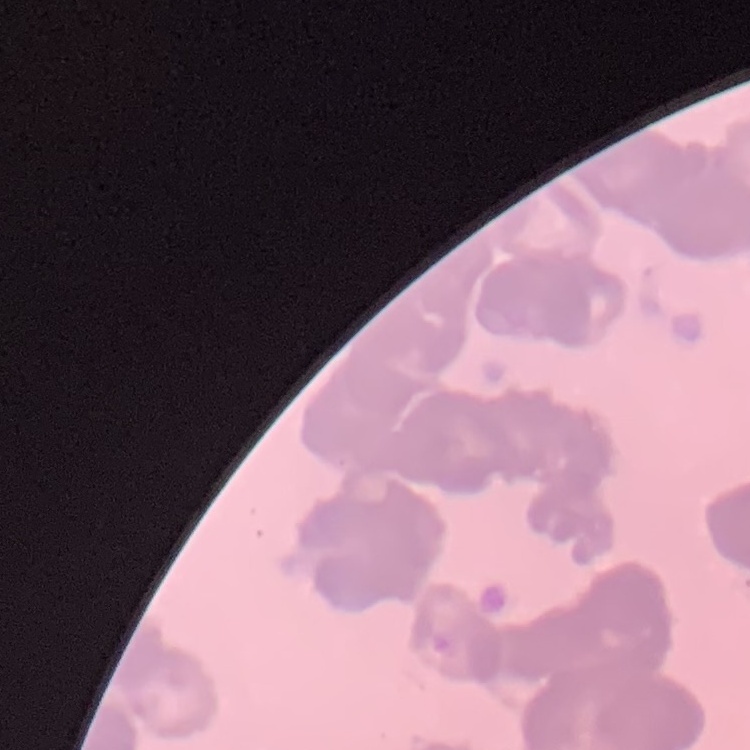
erythrocyte morphology = rouleaux formation
stain = Field's or Giemsa
image type = square crop of a larger photomicrograph
preparation = thin peripheral smear